Assess the morphology of the red blood cells.
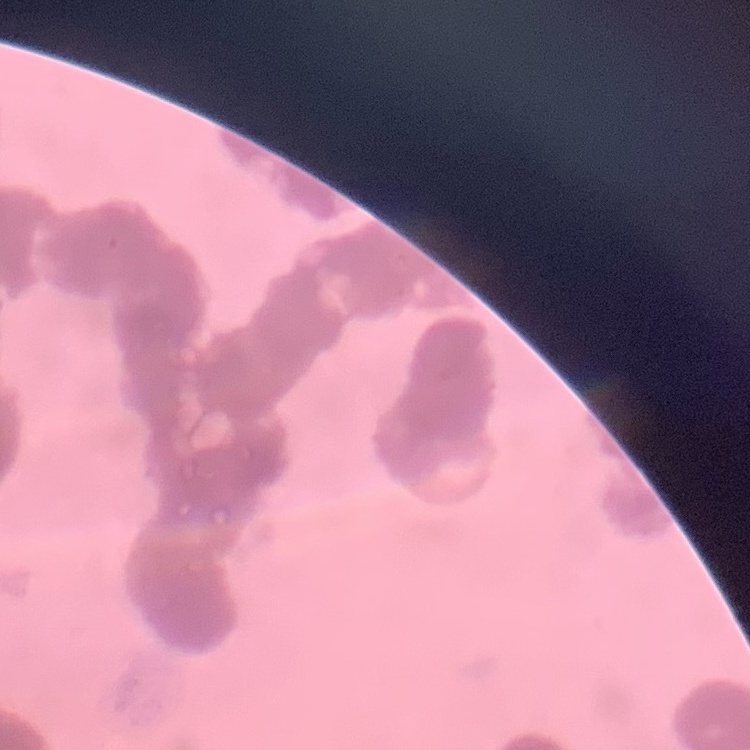

They show rouleaux formation.

Summary:
  - Preparation: thin blood smear
  - Stain: Field's or Giemsa
  - Image type: one tile cut from a larger photomicrograph